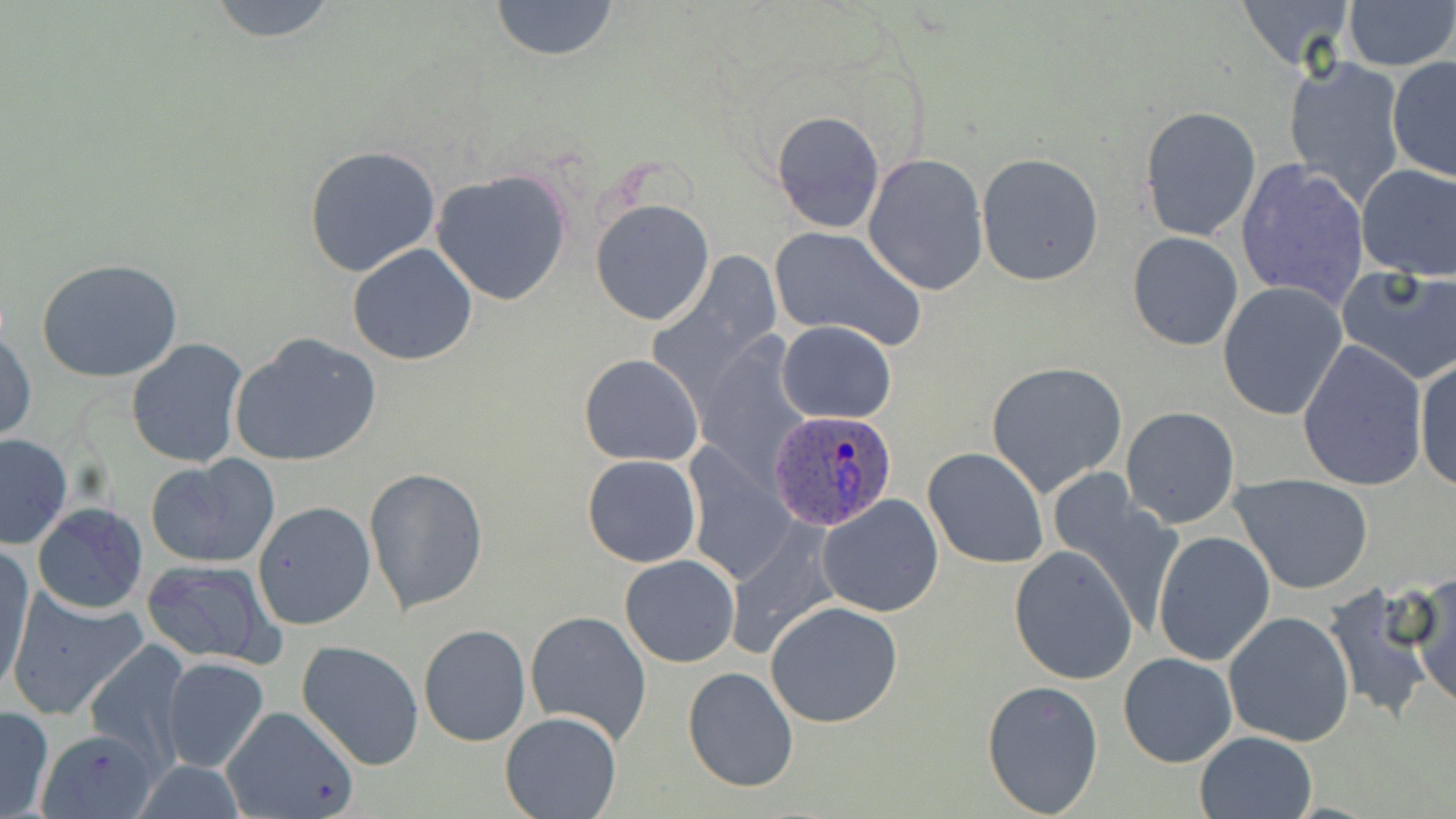
Approximate bounding boxes as (x1, y1, x2, y2) in pixels. Plasmodium ovale-infected red blood cell locations: (769, 409, 898, 532). Uninfected red blood cell locations: (204, 0, 342, 44), (487, 0, 622, 63), (1235, 0, 1357, 73), (1341, 0, 1454, 71), (1282, 55, 1408, 205), (1387, 56, 1456, 182), (1137, 105, 1262, 244), (771, 110, 885, 234), (303, 145, 443, 279), (862, 153, 988, 297), (976, 153, 1106, 288), (1234, 159, 1372, 309), (1355, 163, 1456, 281), (431, 168, 573, 305), (590, 196, 715, 326), (770, 227, 927, 351), (1127, 231, 1244, 350), (347, 243, 479, 366), (36, 258, 184, 382), (1336, 265, 1456, 384), (1217, 283, 1348, 421), (774, 322, 898, 423), (0, 328, 36, 445), (229, 332, 382, 468), (126, 338, 250, 468), (1298, 339, 1428, 490), (579, 354, 704, 467), (1414, 357, 1456, 490), (985, 361, 1129, 498), (1009, 392, 1239, 520), (1122, 406, 1240, 528), (0, 435, 73, 549), (924, 447, 1049, 569), (582, 454, 702, 567), (144, 456, 279, 569), (687, 463, 800, 594), (363, 468, 490, 615), (1231, 472, 1374, 594), (1047, 473, 1188, 634), (817, 494, 945, 618), (252, 501, 375, 629), (32, 503, 148, 613), (725, 522, 845, 660), (1152, 531, 1275, 667), (1, 546, 35, 698), (1009, 546, 1139, 686), (619, 554, 741, 668), (140, 558, 281, 669), (1412, 574, 1456, 712), (1322, 584, 1442, 724), (6, 589, 148, 721), (764, 600, 904, 728), (525, 610, 654, 743), (1223, 611, 1356, 747), (418, 623, 531, 747), (295, 639, 424, 771), (83, 642, 191, 764), (1117, 652, 1237, 768), (159, 657, 270, 773), (682, 666, 799, 794), (982, 679, 1105, 817), (219, 705, 361, 819), (0, 706, 53, 819), (501, 711, 621, 819), (1195, 730, 1316, 818), (35, 731, 147, 819). Slide-level diagnosis: Plasmodium ovale. May-Grünwald-Giemsa-stained preparation. Light microscopy. Image is 1456×819 pixels. Captured at 1000x magnification. Single field of view. Thin blood film.